Outline each Plasmodium falciparum-infected red blood cell.
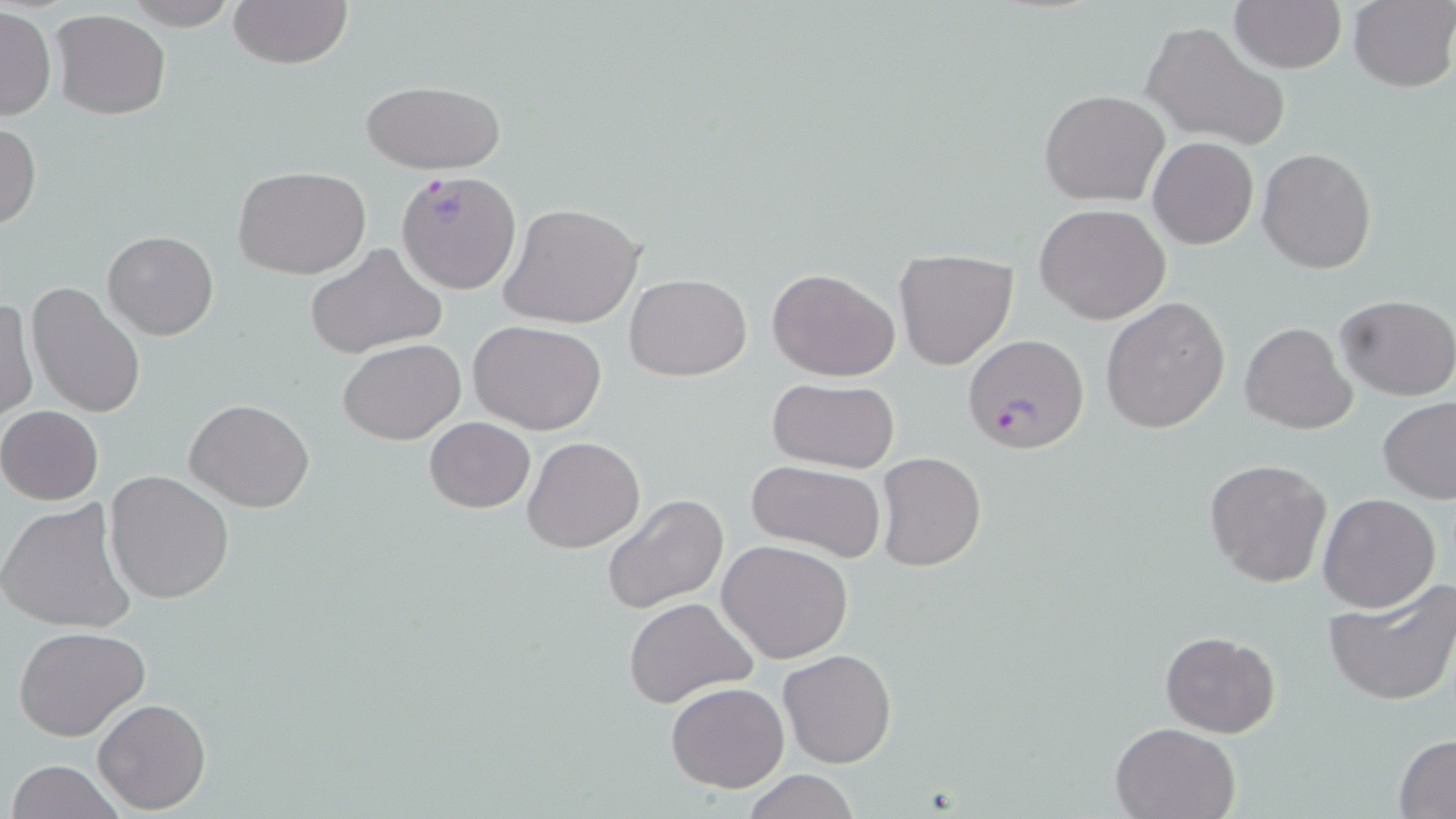

Approximate bounding boxes as (x1, y1, x2, y2) in pixels.
Plasmodium falciparum-infected red blood cells: (396, 172, 521, 296), (963, 337, 1091, 458).

Uninfected red blood cell locations: (121, 0, 240, 29), (228, 0, 350, 69), (1230, 1, 1345, 73), (1347, 1, 1456, 91), (1, 6, 56, 121), (50, 9, 170, 120), (1141, 19, 1287, 150), (360, 80, 509, 175), (1039, 91, 1168, 207), (0, 124, 41, 231), (1148, 137, 1258, 250), (1257, 146, 1377, 274), (233, 167, 371, 278), (500, 202, 648, 331), (1034, 203, 1170, 324), (104, 230, 219, 340), (303, 242, 447, 360), (893, 250, 1018, 369), (767, 266, 900, 381), (624, 273, 751, 381), (25, 282, 147, 418), (1334, 294, 1455, 401), (0, 296, 36, 424), (1101, 297, 1230, 434), (470, 319, 607, 435), (1241, 321, 1357, 435), (337, 337, 466, 445), (766, 378, 901, 474), (1378, 397, 1456, 504), (184, 398, 315, 513), (0, 406, 104, 505), (422, 418, 534, 513), (522, 436, 644, 554), (875, 453, 988, 572), (1203, 459, 1333, 589), (746, 461, 888, 564), (104, 471, 234, 604), (601, 492, 730, 614), (1317, 493, 1440, 613), (0, 497, 137, 635), (718, 540, 855, 663), (1323, 577, 1456, 708), (623, 596, 760, 709), (13, 626, 151, 742), (1160, 630, 1280, 738), (778, 648, 897, 768), (666, 681, 789, 792), (92, 697, 210, 813), (1110, 720, 1241, 818), (1393, 735, 1456, 816), (7, 760, 124, 818), (738, 770, 865, 819). Slide-level diagnosis: Plasmodium falciparum. May-Grünwald-Giemsa stain. Image is 1456×819 pixels. Thin blood smear. Optical microscopy. Captured at 1000x magnification. One field of a larger specimen.